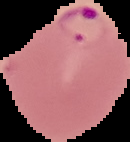

Summary:
  - Preparation: thin blood film
  - Image type: segmented cell region with the area outside set to black
  - Image size: 130×142 pixels
  - Malaria status: parasitized